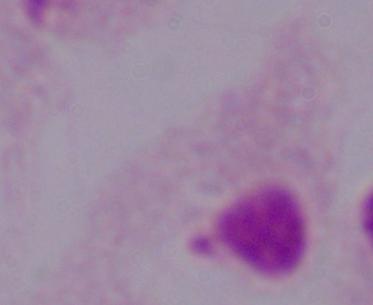

Summary:
  - Modality: photomicrograph
  - Magnification: 1000x
  - Identification: trichomonad